Comment on the morphology of the red blood cells.
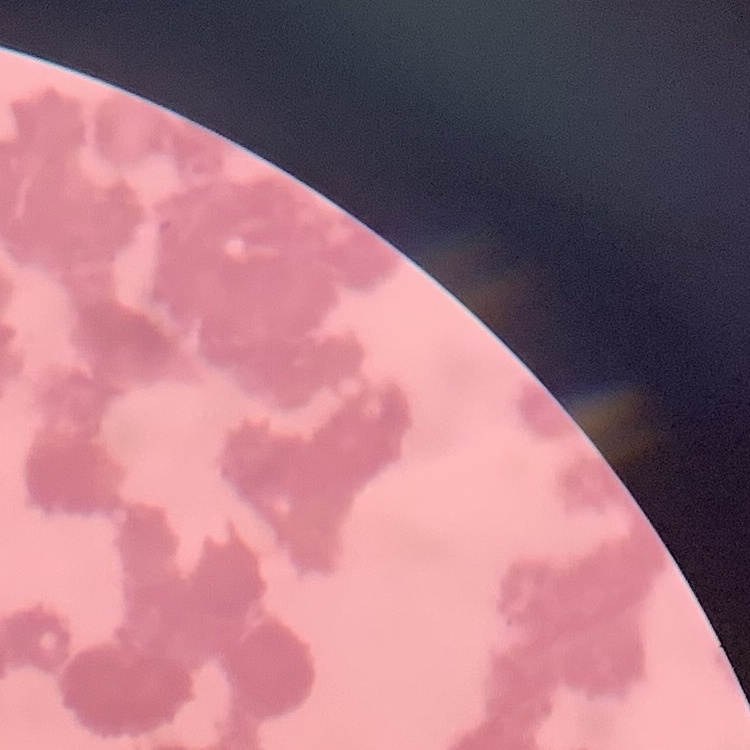
They show rouleaux formation.

preparation = thin peripheral smear
image type = one tile cut from a larger photomicrograph
stain = Field's or Giemsa